Locate every blood parasite and identify its species.
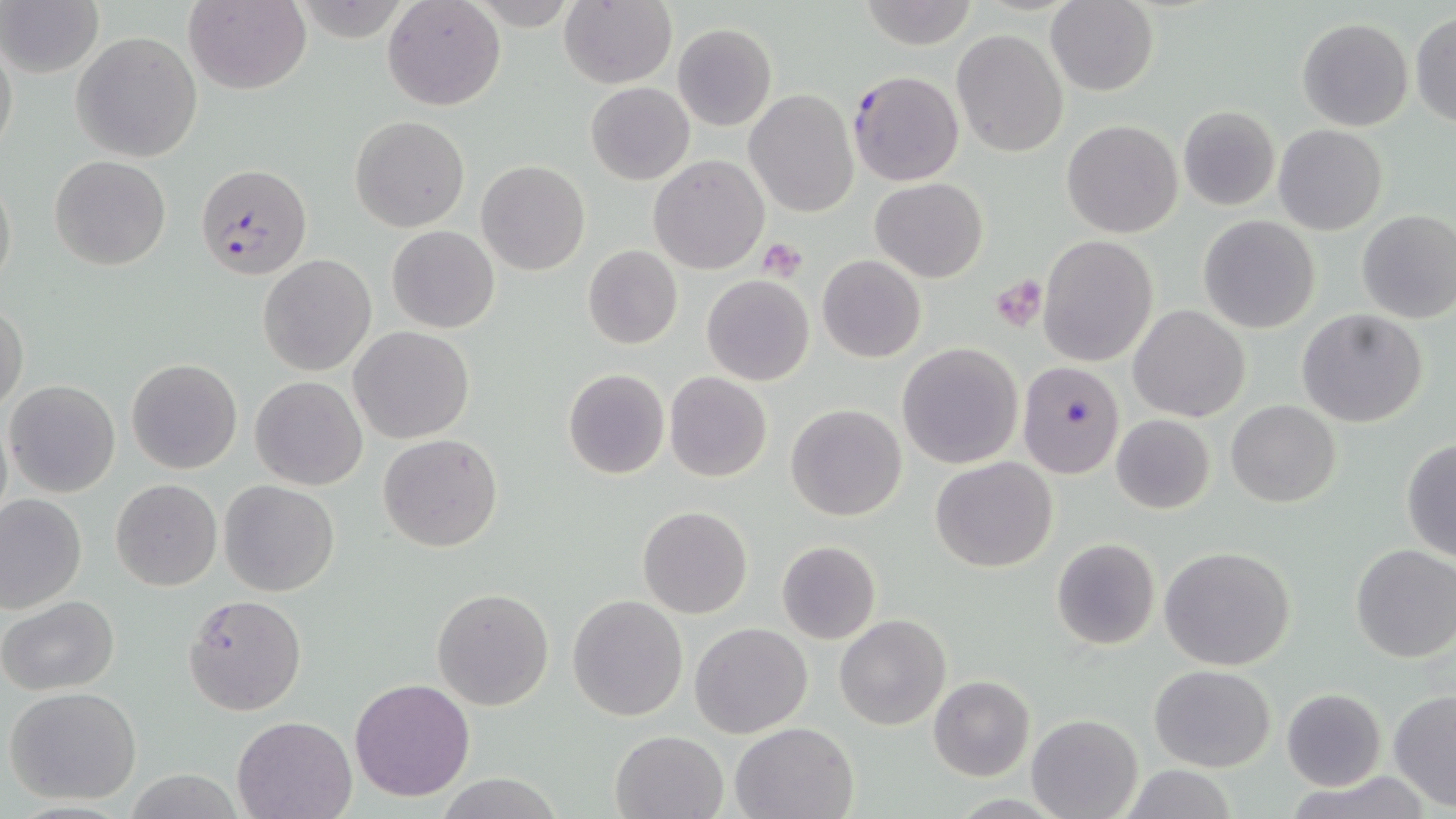
Approximate bounding boxes as named x1/y1/x2/y2 corners in pixels.
Plasmodium falciparum-infected red blood cells: (x1=848, y1=69, x2=963, y2=186), (x1=194, y1=163, x2=312, y2=281), (x1=1017, y1=359, x2=1126, y2=479).
No Plasmodium ovale, Plasmodium malariae, Plasmodium vivax, Babesia divergens, or Trypanosoma brucei observed.

slide-level diagnosis = Plasmodium falciparum
platelet locations = approximate bounding boxes as named x1/y1/x2/y2 corners in pixels: (x1=757, y1=238, x2=807, y2=282), (x1=990, y1=275, x2=1047, y2=331)
uninfected red blood cell locations = approximate bounding boxes as named x1/y1/x2/y2 corners in pixels: (x1=0, y1=0, x2=103, y2=79), (x1=183, y1=0, x2=311, y2=95), (x1=382, y1=0, x2=506, y2=112), (x1=858, y1=0, x2=981, y2=49), (x1=470, y1=1, x2=580, y2=30), (x1=557, y1=1, x2=678, y2=89), (x1=1045, y1=1, x2=1160, y2=97), (x1=1410, y1=11, x2=1456, y2=127), (x1=1297, y1=17, x2=1413, y2=131), (x1=671, y1=24, x2=777, y2=131), (x1=1, y1=28, x2=18, y2=168), (x1=951, y1=30, x2=1068, y2=156), (x1=71, y1=31, x2=203, y2=161), (x1=586, y1=82, x2=694, y2=184), (x1=743, y1=92, x2=859, y2=216), (x1=1178, y1=106, x2=1279, y2=210), (x1=350, y1=116, x2=470, y2=233), (x1=1063, y1=120, x2=1183, y2=237), (x1=1273, y1=124, x2=1389, y2=235), (x1=49, y1=155, x2=172, y2=271), (x1=649, y1=155, x2=770, y2=274), (x1=476, y1=160, x2=590, y2=276), (x1=0, y1=164, x2=16, y2=301), (x1=870, y1=177, x2=988, y2=281), (x1=1356, y1=210, x2=1456, y2=324), (x1=1198, y1=215, x2=1321, y2=334), (x1=387, y1=226, x2=499, y2=333), (x1=1038, y1=234, x2=1159, y2=367), (x1=583, y1=245, x2=682, y2=350), (x1=259, y1=254, x2=376, y2=375), (x1=817, y1=255, x2=926, y2=363), (x1=701, y1=276, x2=814, y2=386), (x1=1, y1=301, x2=27, y2=412), (x1=1129, y1=305, x2=1250, y2=422), (x1=1296, y1=310, x2=1428, y2=428), (x1=348, y1=325, x2=475, y2=443), (x1=896, y1=343, x2=1022, y2=468), (x1=127, y1=357, x2=243, y2=474), (x1=563, y1=368, x2=669, y2=479), (x1=664, y1=372, x2=773, y2=482), (x1=251, y1=375, x2=367, y2=491), (x1=4, y1=379, x2=121, y2=497), (x1=1225, y1=399, x2=1341, y2=507), (x1=786, y1=404, x2=907, y2=520), (x1=1111, y1=414, x2=1215, y2=514), (x1=378, y1=434, x2=504, y2=553), (x1=1400, y1=437, x2=1456, y2=565), (x1=931, y1=456, x2=1058, y2=571), (x1=110, y1=478, x2=222, y2=591), (x1=219, y1=481, x2=341, y2=597), (x1=0, y1=494, x2=87, y2=614), (x1=638, y1=505, x2=752, y2=619), (x1=1051, y1=538, x2=1160, y2=651), (x1=775, y1=540, x2=882, y2=643), (x1=1349, y1=543, x2=1456, y2=663), (x1=1159, y1=545, x2=1296, y2=670), (x1=432, y1=588, x2=554, y2=711), (x1=182, y1=593, x2=306, y2=715), (x1=568, y1=594, x2=687, y2=721), (x1=1, y1=595, x2=120, y2=695), (x1=835, y1=614, x2=952, y2=731), (x1=690, y1=622, x2=813, y2=737), (x1=1149, y1=665, x2=1275, y2=771), (x1=928, y1=676, x2=1035, y2=781), (x1=349, y1=678, x2=475, y2=802), (x1=5, y1=686, x2=143, y2=805), (x1=1281, y1=688, x2=1385, y2=790), (x1=1387, y1=689, x2=1456, y2=812), (x1=1027, y1=714, x2=1141, y2=819), (x1=232, y1=715, x2=358, y2=819), (x1=730, y1=720, x2=859, y2=818), (x1=611, y1=729, x2=728, y2=818), (x1=1116, y1=765, x2=1242, y2=819), (x1=438, y1=773, x2=560, y2=818)
field of view = one of a larger specimen
magnification = 1000x
image size = 1456×819 pixels
modality = optical microscopy
stain = May-Grünwald-Giemsa
preparation = thin blood film